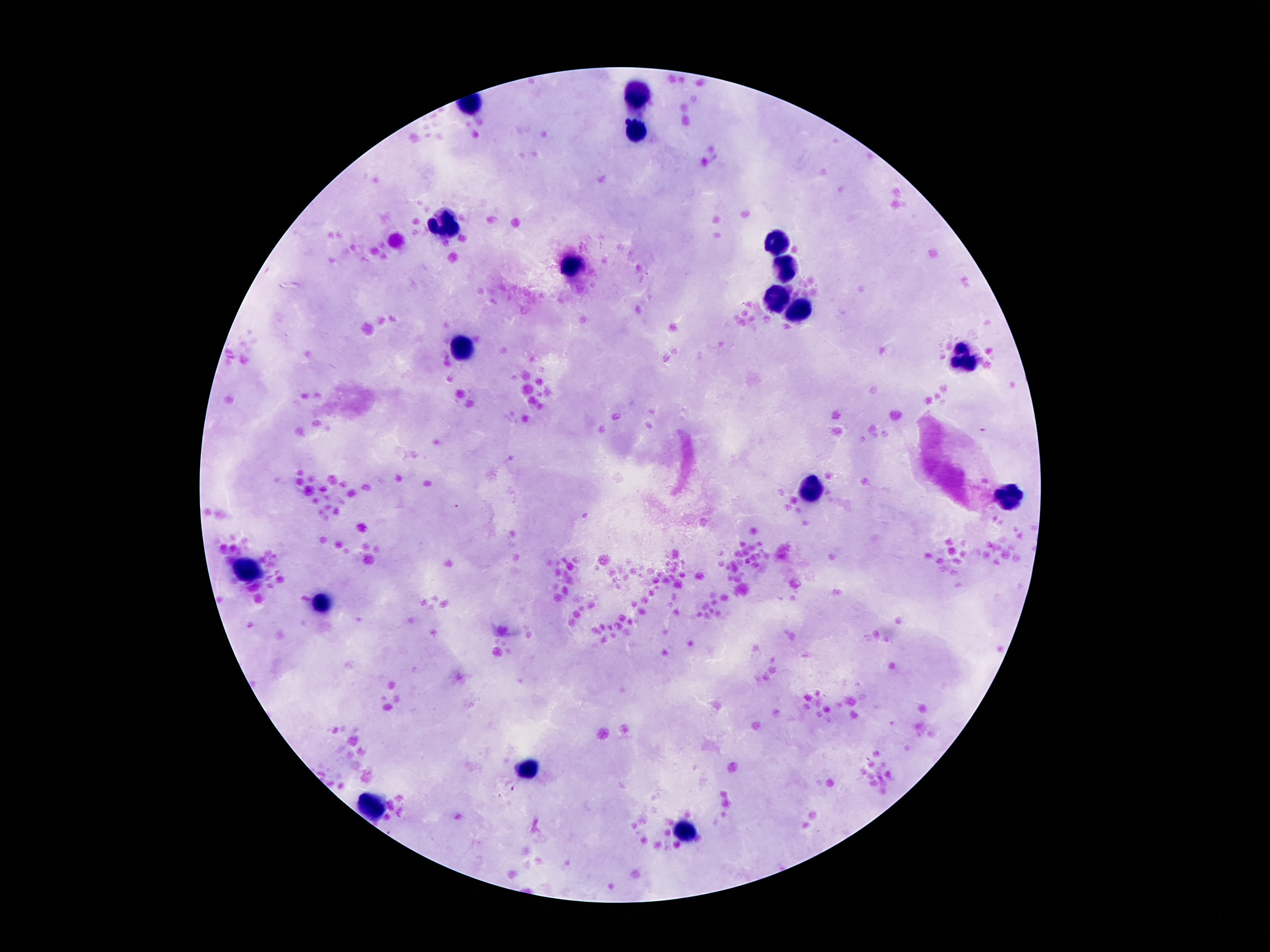
Approximate centers as [x, y] in pixels. Leukocyte locations: [638, 97], [635, 129], [448, 223], [778, 241], [570, 267], [782, 271], [778, 299], [796, 313], [463, 349], [968, 362], [813, 491], [1010, 493], [250, 571], [320, 605], [528, 771], [374, 804], [689, 834]. 100x magnification. Image is 1270×952 pixels. Single field of view. Patient malaria status: negative. Photographed through the microscope eyepiece with a smartphone camera. Thick peripheral-blood smear. Giemsa-stained preparation.